Assess this cell for malaria.
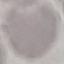
Uninfected.

Cell patch, automatically extracted from a larger field of view and resized to 64 × 64 pixels. Giemsa-stained preparation. Thin blood smear. Acquired by smartphone through the microscope eyepiece.